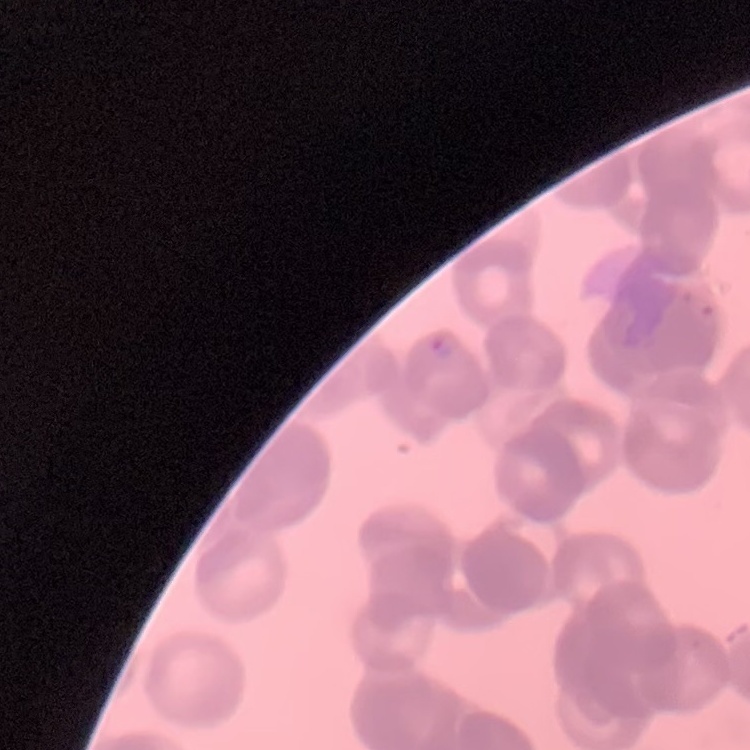
Summary:
  - Red blood cell morphology: rouleaux formation
  - Preparation: thin blood film
  - Stain: Field's or Giemsa
  - Image type: square crop of a larger photomicrograph